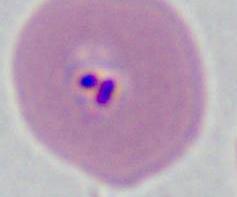

A Plasmodium parasite is shown. Micrograph. Captured at either 400x or 1000x magnification.